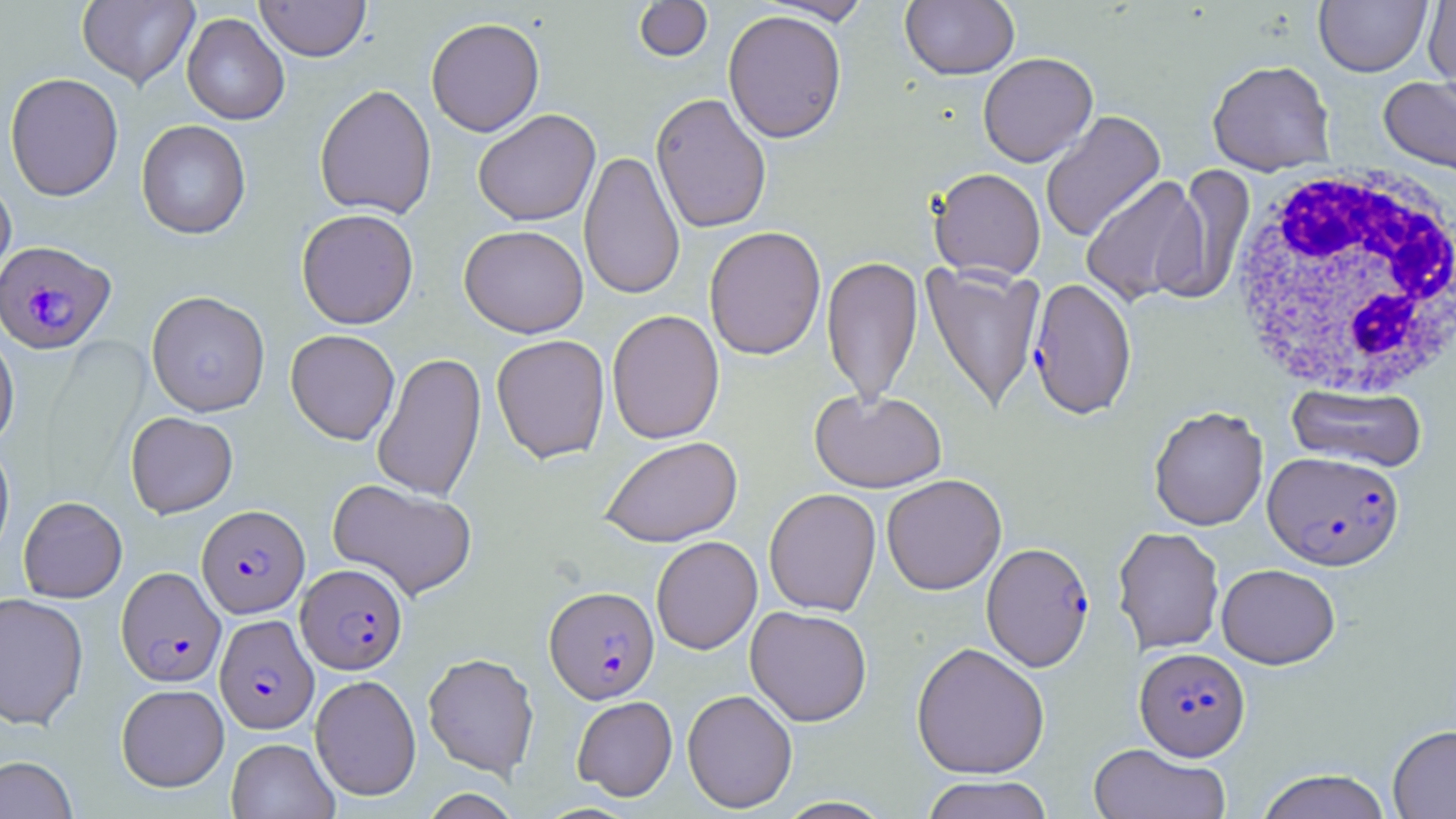
Summary:
  - Coordinate format: approximate bounding boxes as named x1/y1/x2/y2 corners in pixels
  - Plasmodium falciparum-infected red blood cell locations: (x1=0, y1=240, x2=116, y2=354), (x1=1028, y1=277, x2=1137, y2=419), (x1=1263, y1=451, x2=1405, y2=570), (x1=196, y1=504, x2=309, y2=618), (x1=981, y1=542, x2=1095, y2=672), (x1=297, y1=563, x2=408, y2=674), (x1=116, y1=567, x2=226, y2=687), (x1=544, y1=586, x2=659, y2=703), (x1=215, y1=614, x2=319, y2=735), (x1=1134, y1=647, x2=1250, y2=761)
  - Uninfected red blood cell locations: (x1=77, y1=0, x2=199, y2=89), (x1=255, y1=0, x2=371, y2=62), (x1=633, y1=0, x2=713, y2=63), (x1=760, y1=0, x2=874, y2=24), (x1=1314, y1=0, x2=1432, y2=77), (x1=1423, y1=0, x2=1456, y2=91), (x1=900, y1=1, x2=1019, y2=80), (x1=723, y1=9, x2=847, y2=143), (x1=182, y1=13, x2=290, y2=125), (x1=425, y1=17, x2=545, y2=136), (x1=977, y1=52, x2=1098, y2=167), (x1=1207, y1=59, x2=1335, y2=175), (x1=4, y1=72, x2=124, y2=201), (x1=1378, y1=75, x2=1456, y2=181), (x1=314, y1=84, x2=437, y2=220), (x1=651, y1=92, x2=772, y2=233), (x1=473, y1=109, x2=600, y2=226), (x1=1041, y1=110, x2=1165, y2=242), (x1=135, y1=119, x2=251, y2=239), (x1=579, y1=149, x2=685, y2=300), (x1=1162, y1=166, x2=1255, y2=305), (x1=929, y1=167, x2=1046, y2=281), (x1=0, y1=174, x2=16, y2=295), (x1=1081, y1=175, x2=1208, y2=306), (x1=296, y1=208, x2=419, y2=330), (x1=459, y1=225, x2=589, y2=338), (x1=704, y1=226, x2=826, y2=360), (x1=821, y1=256, x2=923, y2=407), (x1=922, y1=262, x2=1045, y2=414), (x1=146, y1=290, x2=271, y2=417), (x1=607, y1=309, x2=725, y2=444), (x1=0, y1=325, x2=19, y2=452), (x1=285, y1=329, x2=400, y2=445), (x1=491, y1=334, x2=611, y2=464), (x1=372, y1=351, x2=487, y2=502), (x1=1287, y1=383, x2=1427, y2=472), (x1=810, y1=388, x2=947, y2=493), (x1=1148, y1=406, x2=1269, y2=531), (x1=125, y1=411, x2=238, y2=518), (x1=600, y1=436, x2=742, y2=547), (x1=0, y1=440, x2=15, y2=562), (x1=881, y1=474, x2=1006, y2=595), (x1=327, y1=478, x2=478, y2=600), (x1=763, y1=488, x2=882, y2=616), (x1=18, y1=496, x2=127, y2=602), (x1=1112, y1=526, x2=1225, y2=655), (x1=651, y1=535, x2=762, y2=655), (x1=1216, y1=563, x2=1340, y2=669), (x1=0, y1=592, x2=89, y2=730), (x1=745, y1=605, x2=872, y2=726), (x1=911, y1=641, x2=1050, y2=779), (x1=423, y1=652, x2=539, y2=778), (x1=310, y1=674, x2=422, y2=801), (x1=116, y1=683, x2=229, y2=792), (x1=682, y1=689, x2=798, y2=813), (x1=572, y1=696, x2=677, y2=801), (x1=1387, y1=724, x2=1456, y2=818), (x1=226, y1=737, x2=339, y2=819), (x1=1088, y1=742, x2=1231, y2=819), (x1=0, y1=755, x2=78, y2=819), (x1=1256, y1=769, x2=1393, y2=819), (x1=920, y1=774, x2=1053, y2=819), (x1=419, y1=789, x2=522, y2=818), (x1=774, y1=797, x2=895, y2=819)
  - White blood cell locations: (x1=1226, y1=163, x2=1456, y2=400)
  - Slide-level diagnosis: Plasmodium falciparum
  - Magnification: 1000x
  - Modality: optical microscopy
  - Image size: 1456×819 pixels
  - Stain: May-Grünwald-Giemsa
  - Preparation: thin blood film
  - Field of view: single